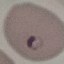
Result: malaria parasites identified. Cell patch, automatically extracted from a larger field of view and resized to 64 × 64 pixels. Acquired by smartphone through the microscope eyepiece. Thin blood smear. Giemsa stain.